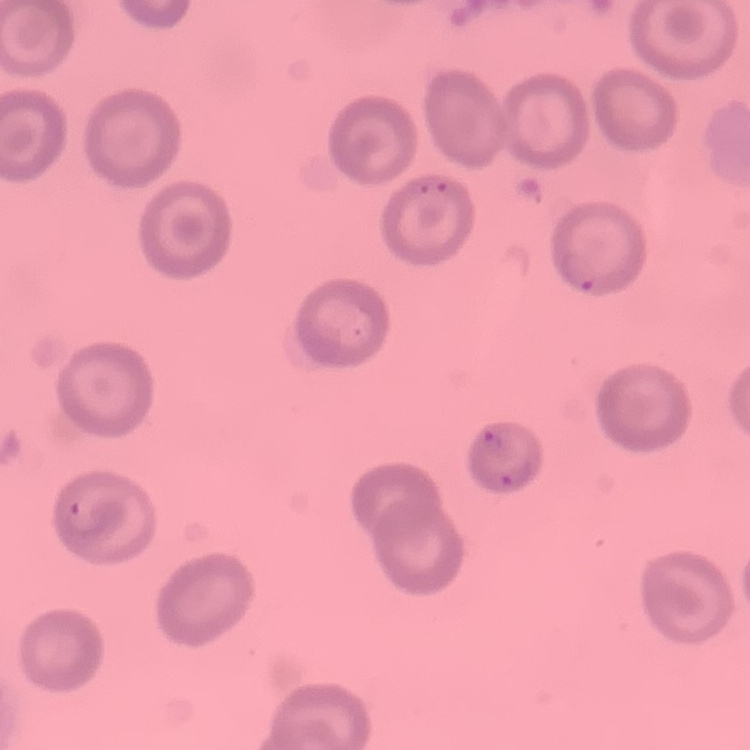 The erythrocytes show no rouleaux formation. Stained with either Field's or Giemsa. One tile cut from a larger photomicrograph. Thin peripheral smear.